Name the cell type shown.
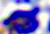

A leukocyte.

400x magnification. Micrograph.